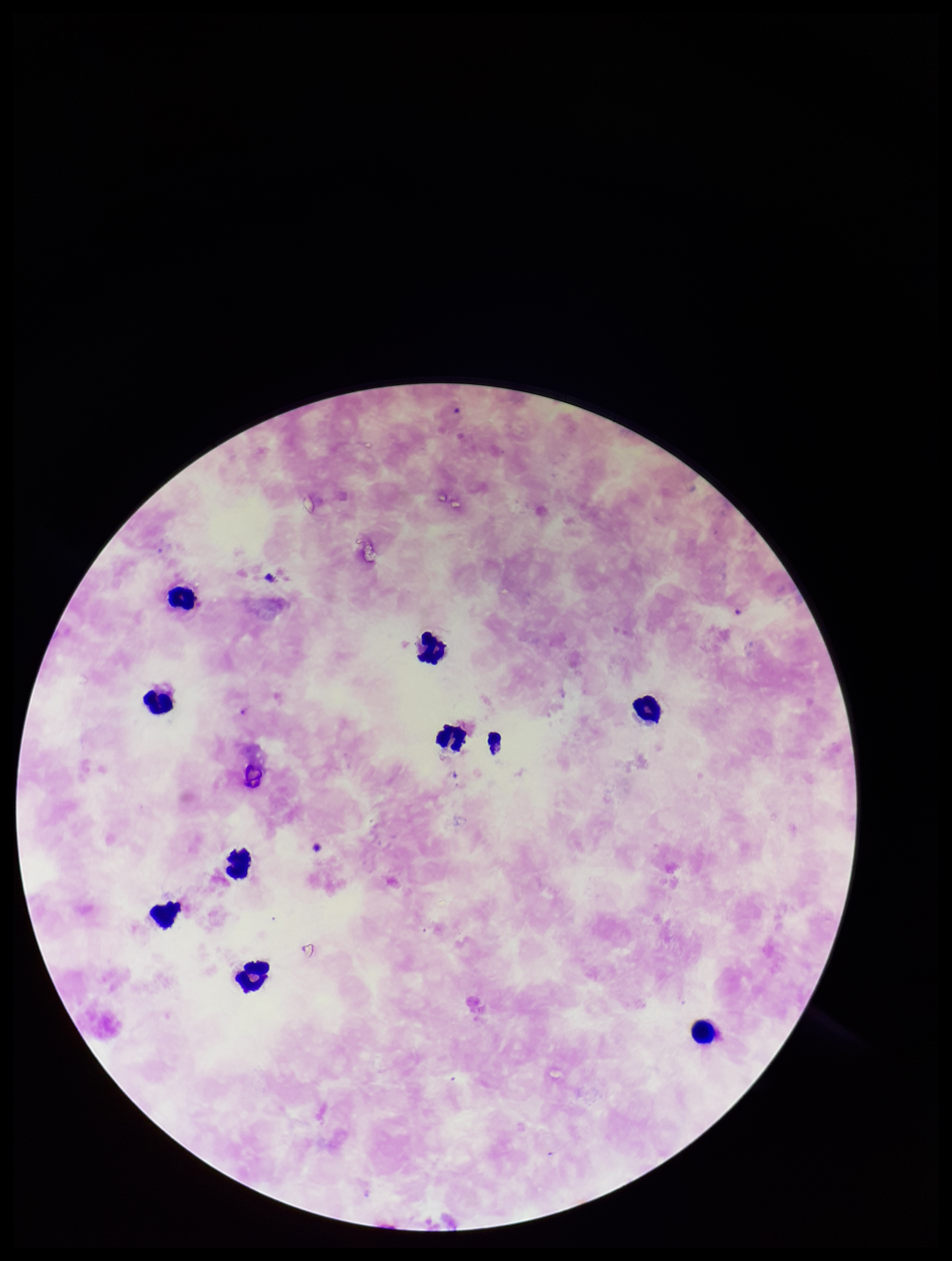 Photographed through the microscope eyepiece with a smartphone camera. Preparation: thick. Parasite count: 0. Single field of view. Leukocyte count: 9. Plasmodium parasites: none detected. Species reported for this patient: Plasmodium falciparum. Patient malaria status: positive. Image is 952×1261 pixels. Stained with Giemsa.